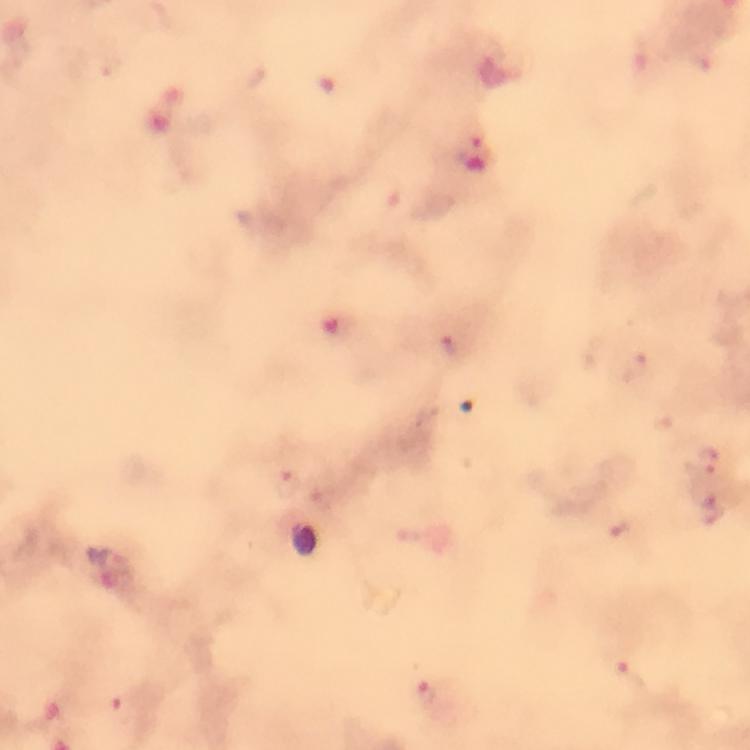
Approximate centers as (x, y) in pixels.
Summary:
  - Malaria parasite locations: (475, 135), (451, 344), (633, 369), (705, 459), (287, 483), (711, 508), (619, 528), (632, 675), (426, 693), (121, 706)
  - Immersion oil: used
  - Image size: 750×750 pixels
  - Cropped from: a single field of view
  - Stain: Giemsa
  - Magnification: 100x
  - Capture: smartphone camera through the microscope
  - Context: from a malaria diagnostic workup
  - Preparation: thick blood smear